Comment on the morphology of the erythrocytes.
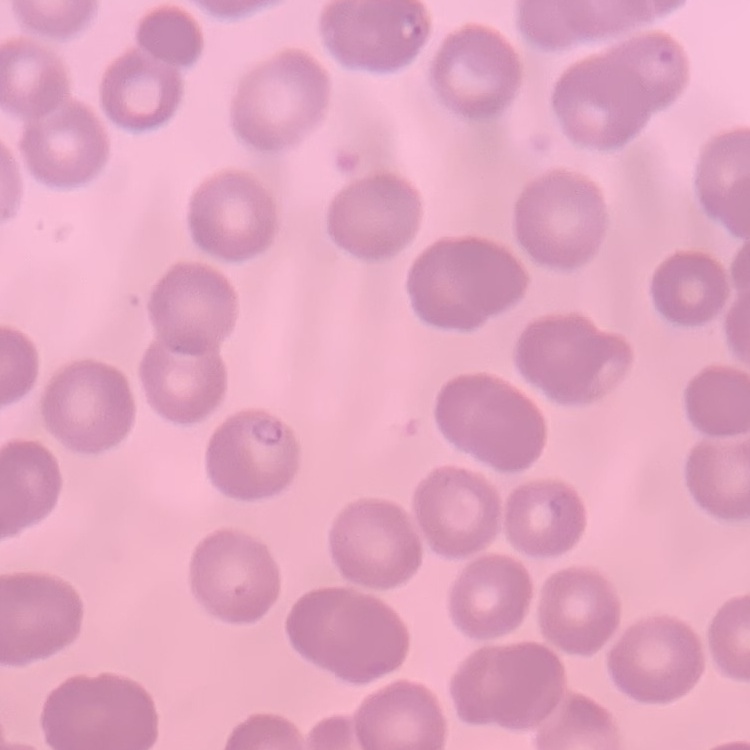
No rouleaux formation.

Stained with either Field's or Giemsa. Square crop of a larger photomicrograph. Thin peripheral smear.